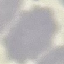
Summary:
  - Result: no malaria parasites detected
  - Capture: smartphone through the microscope eyepiece
  - Preparation: thin smear
  - Stain: Giemsa
  - Image type: cell patch, automatically extracted from a larger field of view and resized to 64 × 64 pixels